Report the malaria status of this cell.
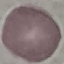
It is uninfected.

Thin blood film. Acquired by smartphone through the microscope eyepiece. Automatically extracted cell patch, resized to 64 × 64 pixels. Giemsa stain.